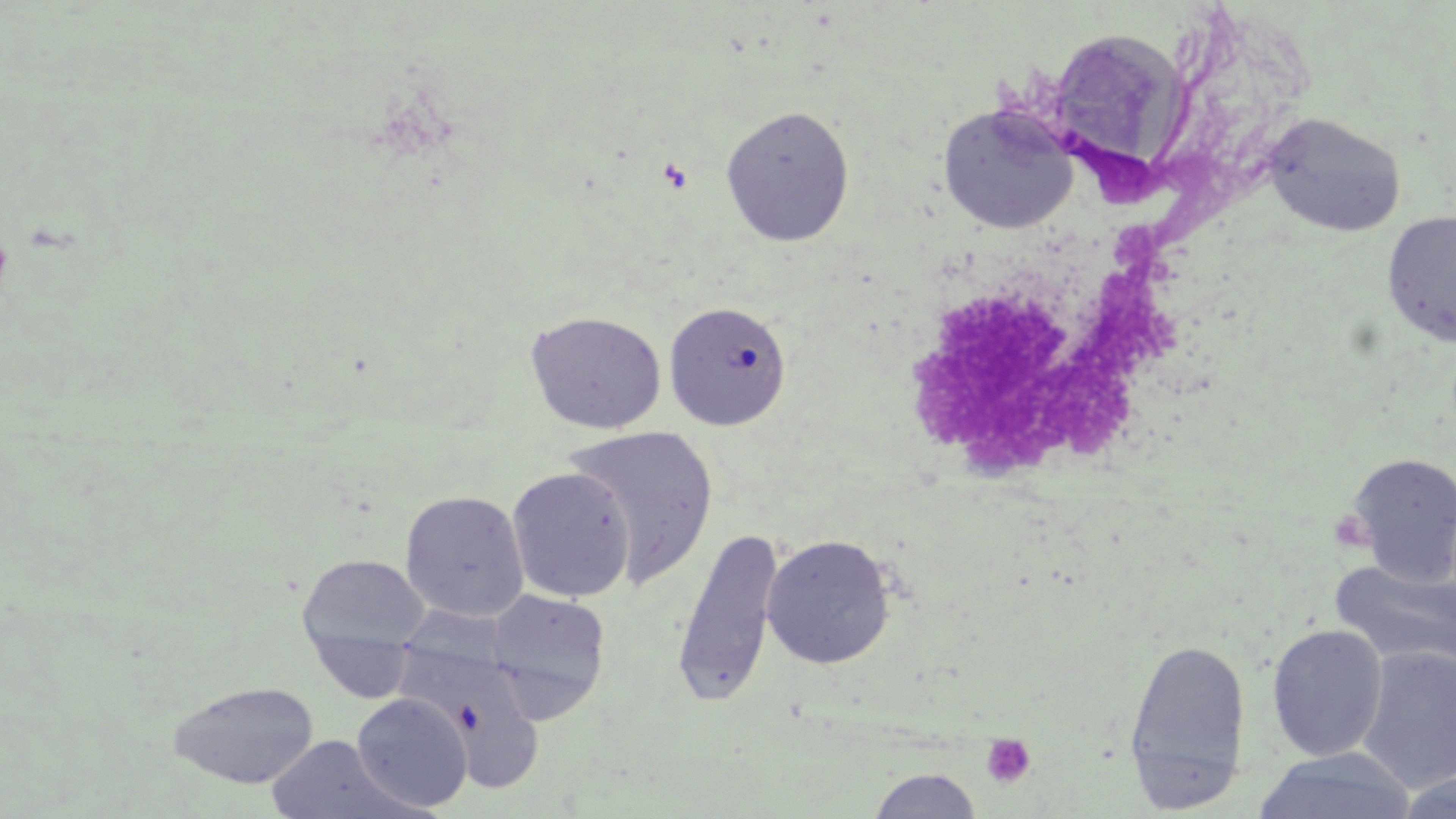

Summary:
  - Coordinate format: approximate bounding boxes as (x1,y1)-(x2,y2) corner pairs in pixels
  - Uninfected red blood cell locations: (937,101)-(1080,235), (719,104)-(855,246), (1262,112)-(1407,237), (1382,211)-(1456,347), (663,301)-(792,431), (525,311)-(667,434), (562,423)-(719,587), (1344,451)-(1456,585), (507,467)-(635,603), (399,490)-(529,622), (671,526)-(786,708), (761,534)-(896,669), (296,553)-(431,671), (1328,556)-(1456,677), (485,589)-(611,721), (1266,624)-(1388,761), (391,635)-(551,793), (1122,636)-(1251,809), (1357,646)-(1456,792), (167,679)-(320,789), (354,693)-(476,812), (264,735)-(414,819), (1253,747)-(1419,819), (867,767)-(982,819), (1391,769)-(1456,818)
  - Platelet locations: (1328,510)-(1377,554), (981,733)-(1037,787)
  - Slide-level diagnosis: negative for blood parasites
  - Magnification: 1000x
  - Modality: light microscopy
  - Preparation: thin blood film
  - Image size: 1456×819 pixels
  - Stain: May-Grünwald-Giemsa
  - Field of view: one of a larger specimen